Report the malaria status of this cell.
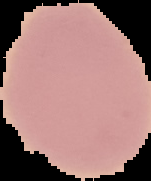

It is uninfected.

The area outside the segmented cell region is set to black. Image is 151×181 pixels. From a thin blood film.